Assess this cell for malaria.
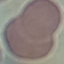
It is uninfected.

Cell patch, automatically extracted from a larger field of view and resized to 64 × 64 pixels. Acquired by smartphone through the microscope eyepiece. Thin blood smear. Giemsa-stained preparation.